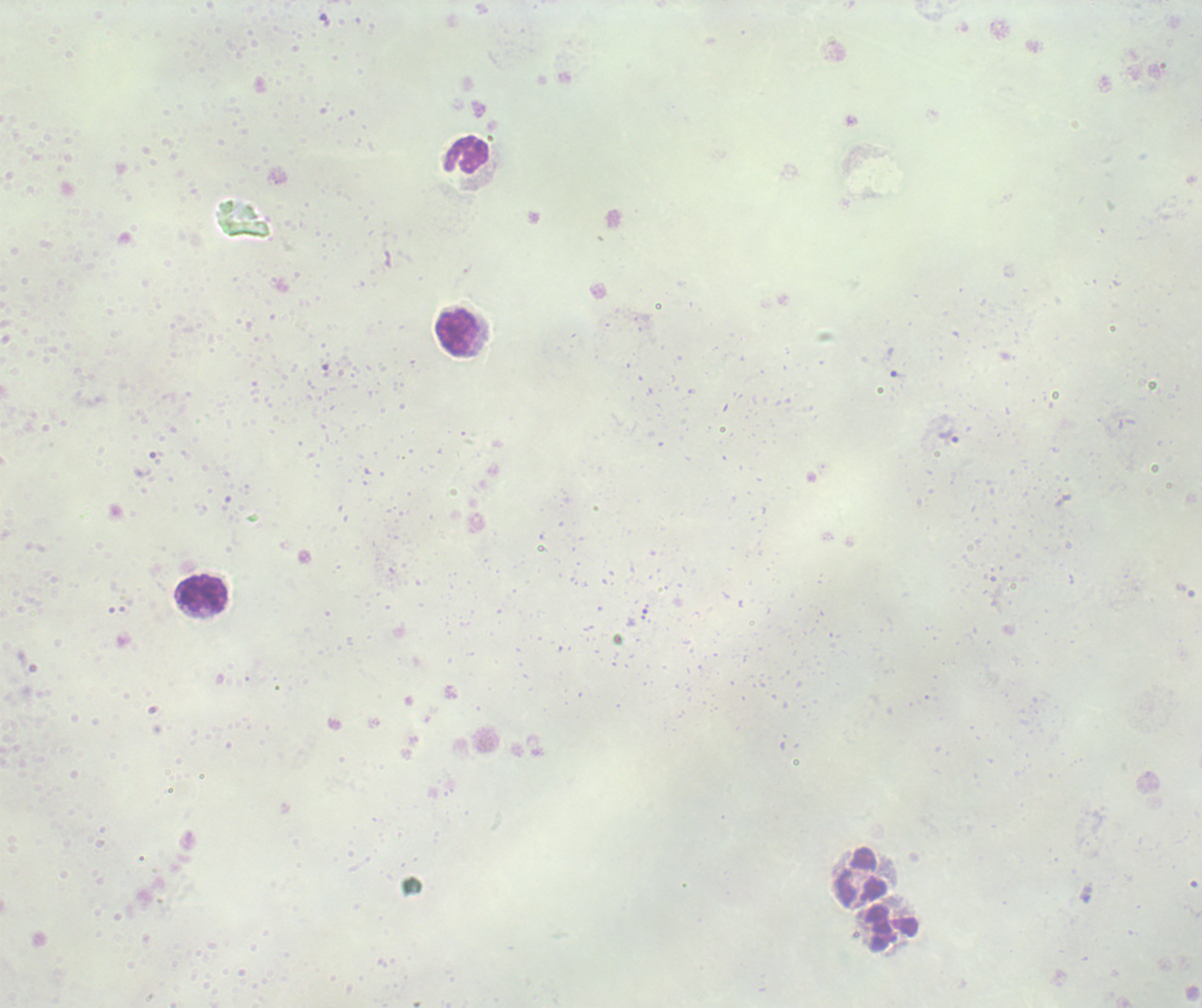
leukocyte_locations: 'approximate centers as (x, y) in pixels: (469, 155), (458, 334), (202, 595), (861, 878), (892, 927)'
trophozoite_locations: 'approximate centers as (x, y) in pixels: (897, 373), (947, 437)'
coloration_quality: bad
context: previously used in an actual diagnosis
field_of_view: single
background_quality: poor
preparation: thick blood film
magnification: 100x
result: malaria parasites detected
image_size: 1202×1008 pixels
stain: Romanowsky